Comment on the morphology of the erythrocytes.
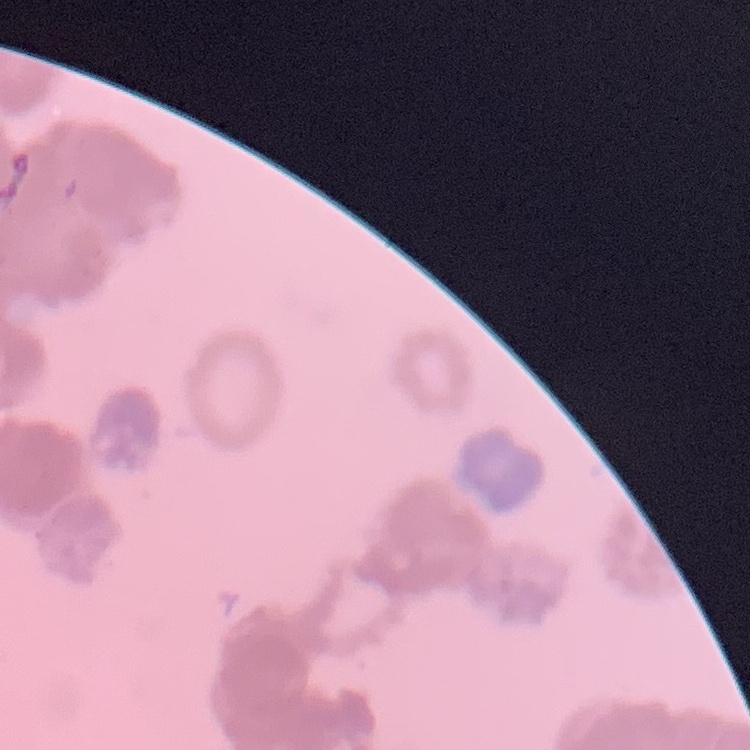

Rouleaux formation.

Thin blood smear. One tile cut from a larger photomicrograph. Stained with either Field's or Giemsa.